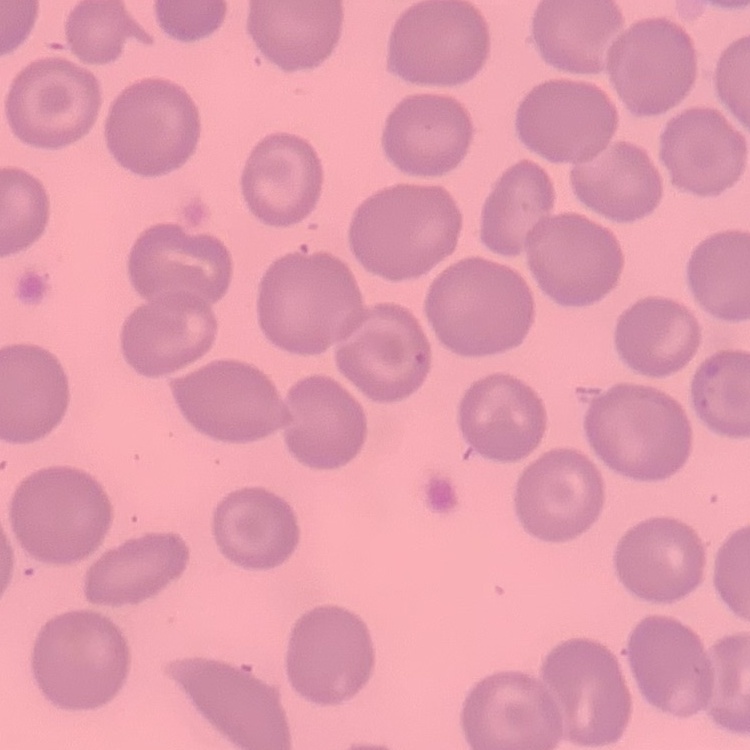 The erythrocytes exhibit no rouleaux formation. Square crop of a larger photomicrograph. Field's or Giemsa stain. Thin peripheral smear.